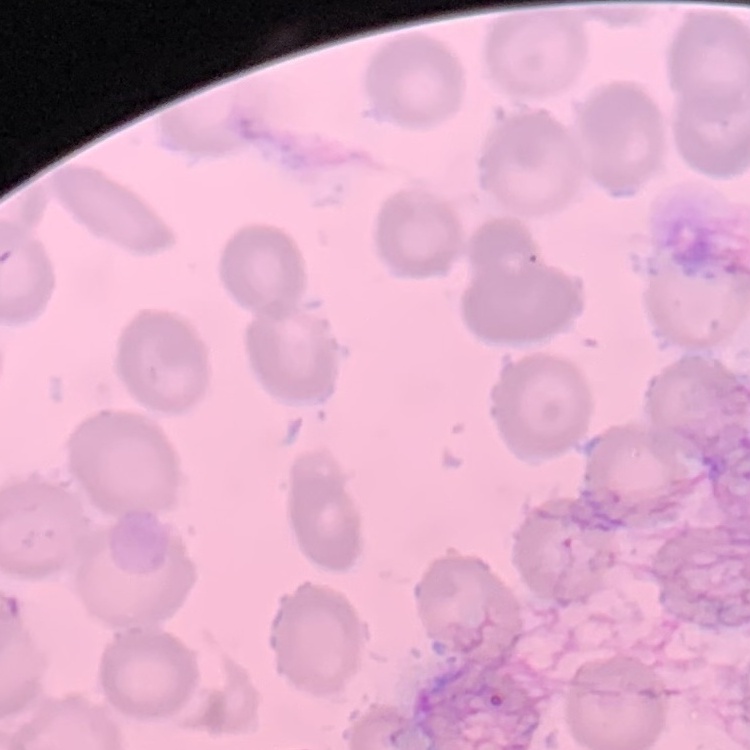

red blood cell morphology = no rouleaux formation
stain = Field's or Giemsa
preparation = thin blood film
image type = square crop of a larger photomicrograph